Point out each Plasmodium parasite.
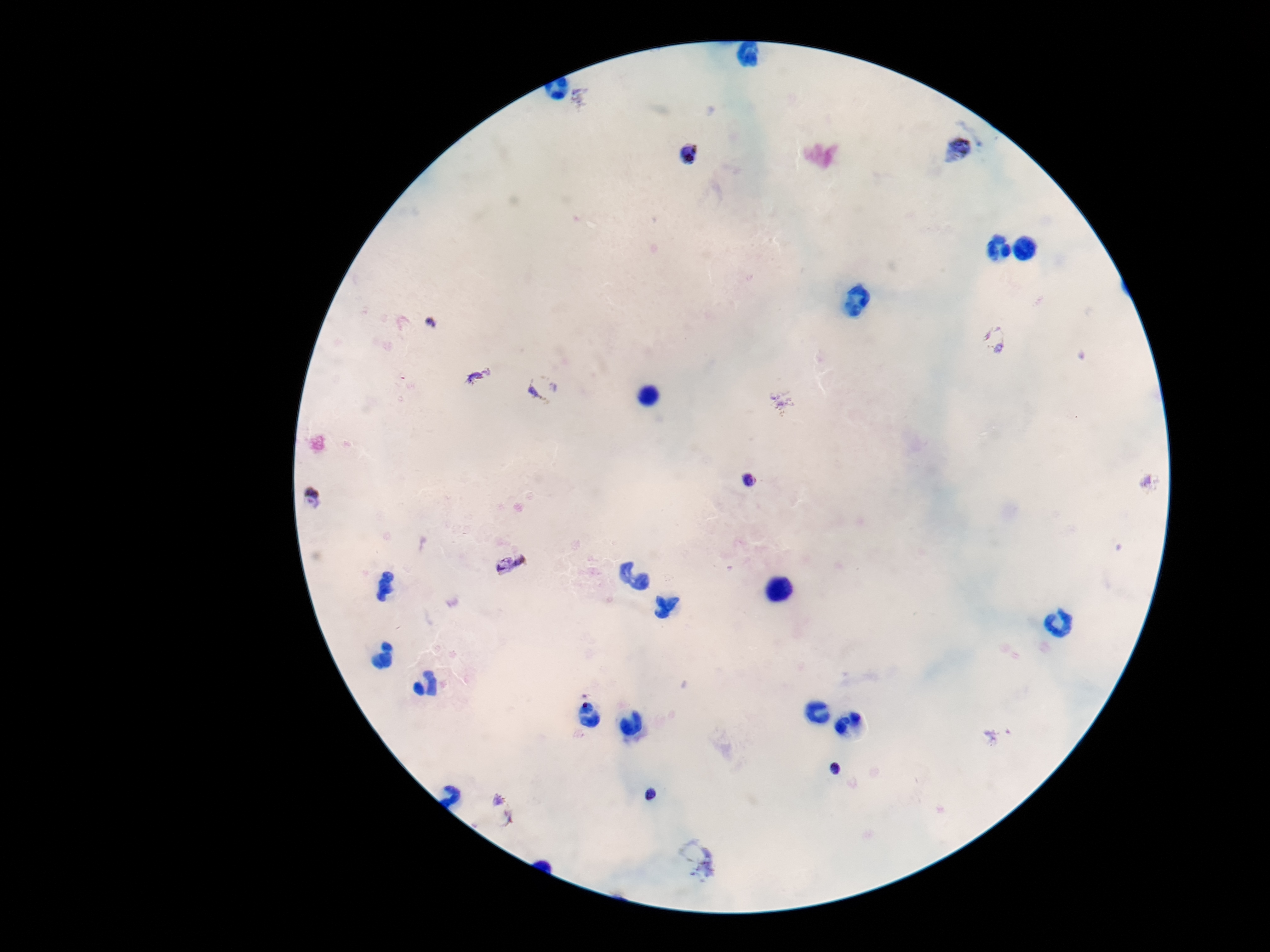

Approximate object centers, in pixels from the top-left corner.
Plasmodium parasites: (x=975, y=129), (x=955, y=155), (x=691, y=156), (x=431, y=323), (x=994, y=339), (x=478, y=376), (x=543, y=387), (x=783, y=399), (x=750, y=481), (x=1150, y=483), (x=312, y=499), (x=511, y=565), (x=999, y=735), (x=836, y=769), (x=650, y=794), (x=503, y=812), (x=697, y=858).

patient malaria status = positive
image size = 1270×952 pixels
capture = smartphone camera through the microscope eyepiece
magnification = 100x
preparation = thick peripheral-blood smear
stain = Giemsa
field of view = single